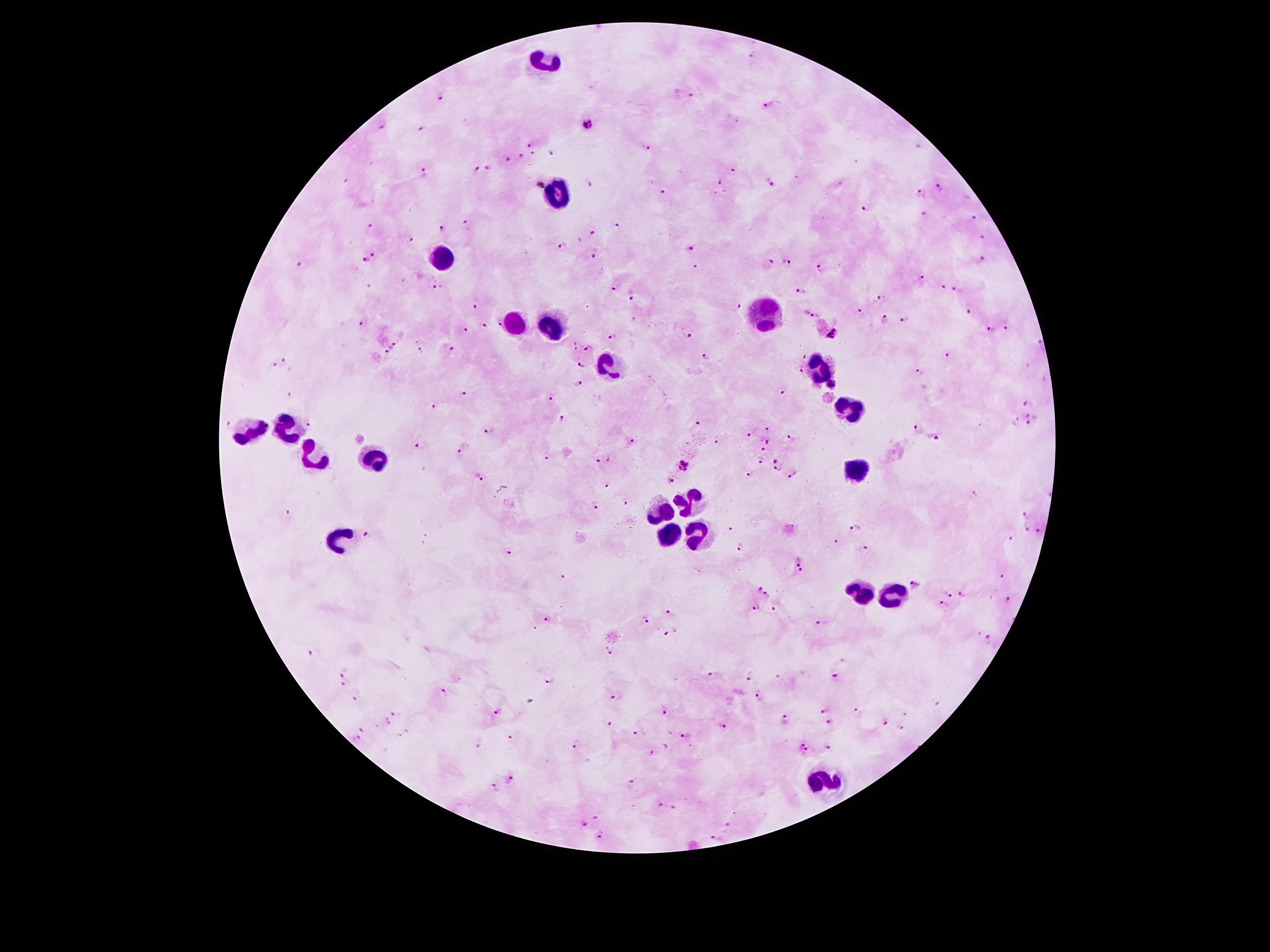

Patient malaria status: positive for Plasmodium falciparum. 100x magnification. Single field of view. Thick blood smear. Photographed through the microscope eyepiece with a smartphone camera. Image is 1270×952 pixels. Giemsa-stained preparation.